Name the parasite shown.
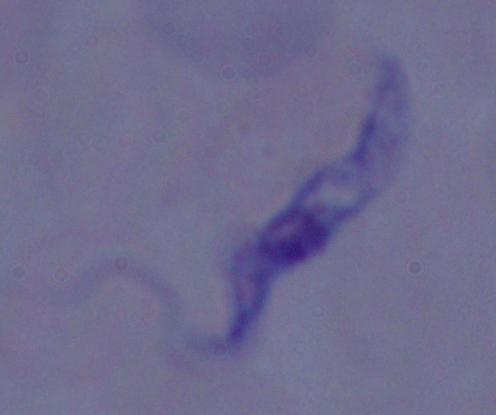
This is a trypanosome.

{
  "magnification": "1000x",
  "modality": "photomicrograph"
}